Assess this cell for malaria.
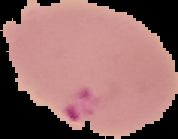

Parasitized.

Summary:
  - Image size: 178×139 pixels
  - Preparation: thin blood smear
  - Image type: segmented cell region on a black background